Classify this cell by malaria status.
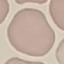
It is uninfected.

Summary:
  - Stain: Giemsa
  - Image type: cell patch, automatically extracted from a larger field of view and resized to 64 × 64 pixels
  - Preparation: thin blood smear
  - Capture: smartphone camera at the microscope eyepiece